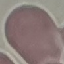

Summary:
  - Result: negative for malaria parasites
  - Capture: smartphone camera at the microscope eyepiece
  - Image type: automatically extracted cell patch, resized to 64 × 64 pixels
  - Preparation: thin smear
  - Stain: Giemsa